Give the location of every parasitized RBC.
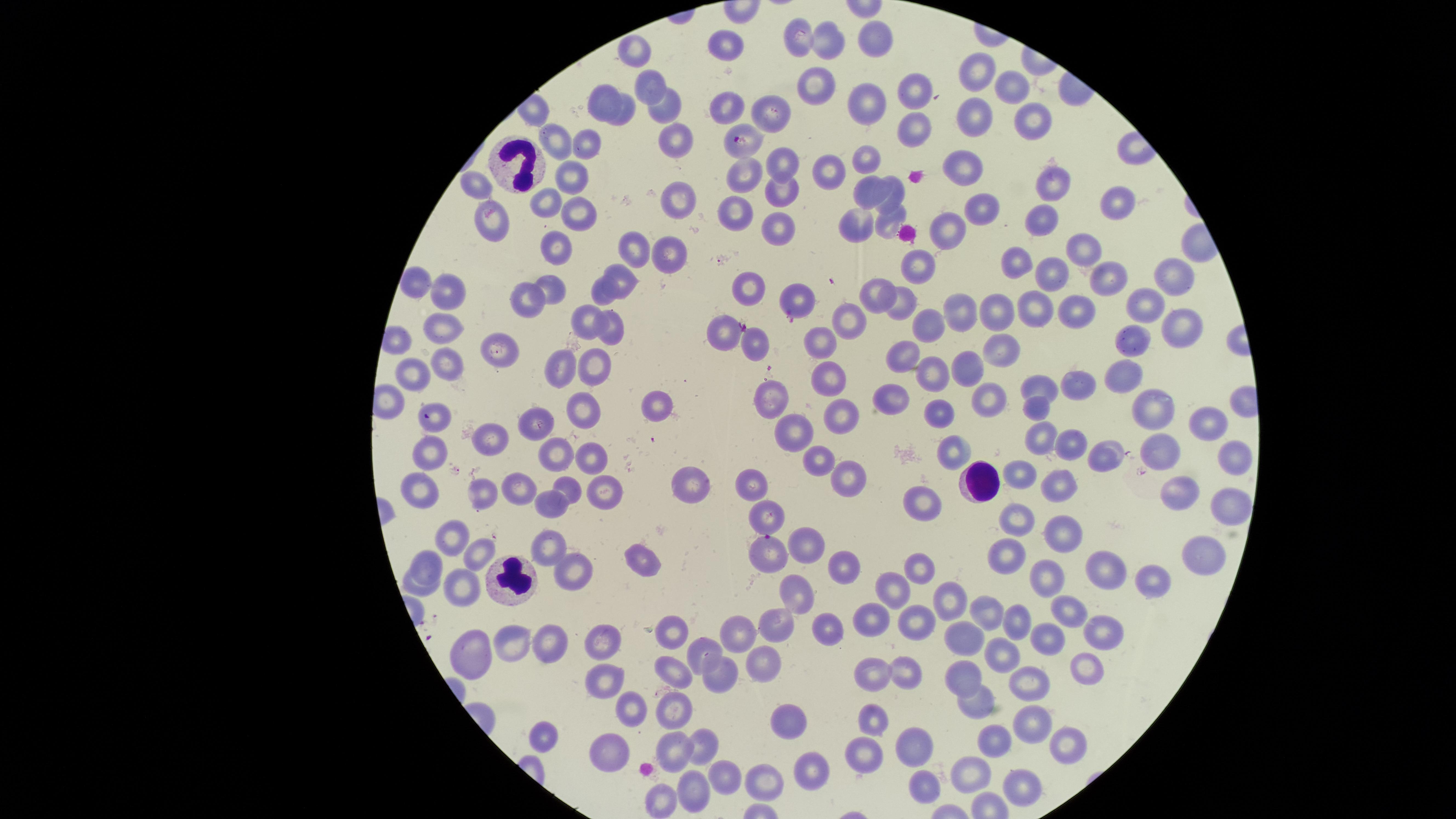

Approximate marker points as [x, y] in pixels.
Parasitized RBCs: [741, 139], [433, 415], [767, 550].

Approximate marker points as [x, y] in pixels. Uninfected RBCs: [799, 36], [877, 37], [726, 43], [830, 43], [634, 48], [979, 69], [646, 84], [1015, 85], [812, 89], [917, 91], [605, 92], [866, 100], [729, 101], [667, 112], [772, 113], [976, 114], [626, 115], [1032, 120], [911, 131], [552, 138], [676, 140], [584, 145], [866, 154], [781, 160], [967, 163], [826, 172], [572, 174], [747, 175], [1052, 180], [477, 186], [870, 187], [896, 190], [783, 192], [682, 194], [1117, 199], [544, 204], [981, 206], [577, 209], [734, 209], [1040, 216], [493, 220], [892, 221], [857, 223], [777, 226], [947, 233], [556, 243], [673, 247], [639, 248], [1080, 250], [1014, 255], [915, 260], [1053, 272], [1109, 272], [624, 277], [1173, 279], [418, 282], [554, 284], [752, 287], [449, 291], [602, 293], [880, 294], [1142, 298], [523, 301], [794, 303], [905, 303], [960, 306], [1076, 306], [1000, 307], [1033, 307], [587, 317], [847, 318], [933, 324], [612, 326], [442, 327], [1184, 329], [724, 332], [1138, 341], [827, 342], [756, 345], [499, 352], [901, 353], [999, 353], [598, 362], [448, 364], [414, 365], [560, 365], [965, 366], [934, 372], [830, 376], [1120, 376], [1073, 383], [1036, 384], [894, 392], [773, 397], [993, 399], [1152, 404], [583, 405], [658, 405], [1038, 405], [842, 409], [940, 412], [1215, 419], [791, 424], [542, 425], [494, 436], [1043, 439], [1079, 447], [951, 448], [1168, 449], [426, 451], [1112, 455], [554, 457], [1235, 457], [586, 458], [820, 459], [848, 476], [1022, 477], [703, 480], [754, 484], [1050, 484], [519, 486], [572, 492], [605, 492], [419, 493], [1185, 494], [483, 495], [555, 505], [922, 506], [1231, 509], [767, 512], [1013, 517], [1057, 526], [459, 534], [551, 543], [810, 543], [481, 547], [1200, 551], [1010, 555], [432, 558], [646, 562], [848, 566], [917, 566], [1097, 566], [571, 567], [1047, 576], [1156, 577], [896, 587], [422, 591], [459, 592], [799, 595], [946, 599], [990, 610], [1071, 611], [1022, 617], [779, 620], [875, 621], [920, 622], [743, 628], [1103, 628], [672, 634], [1050, 637], [975, 638], [548, 641], [606, 642], [512, 645], [472, 648], [701, 649], [1005, 651], [1086, 659], [761, 665], [875, 668], [675, 673], [905, 673], [971, 673], [713, 676], [611, 680], [1021, 680], [631, 707], [981, 708], [678, 713], [874, 715], [1036, 717], [789, 726], [543, 734], [702, 742], [997, 742], [1067, 744], [677, 748], [613, 750], [913, 753], [867, 755], [811, 769], [974, 772], [726, 778], [767, 779], [1024, 779], [925, 784], [695, 785], [663, 800]. WBCs: [514, 158], [979, 481], [514, 584]. Giemsa stain. Thin blood film. One field of view of the specimen. Species: Plasmodium falciparum. Smartphone photograph through the microscope eyepiece. Image is 1456×819 pixels. The visible region is circular.